Identify the blood parasite species.
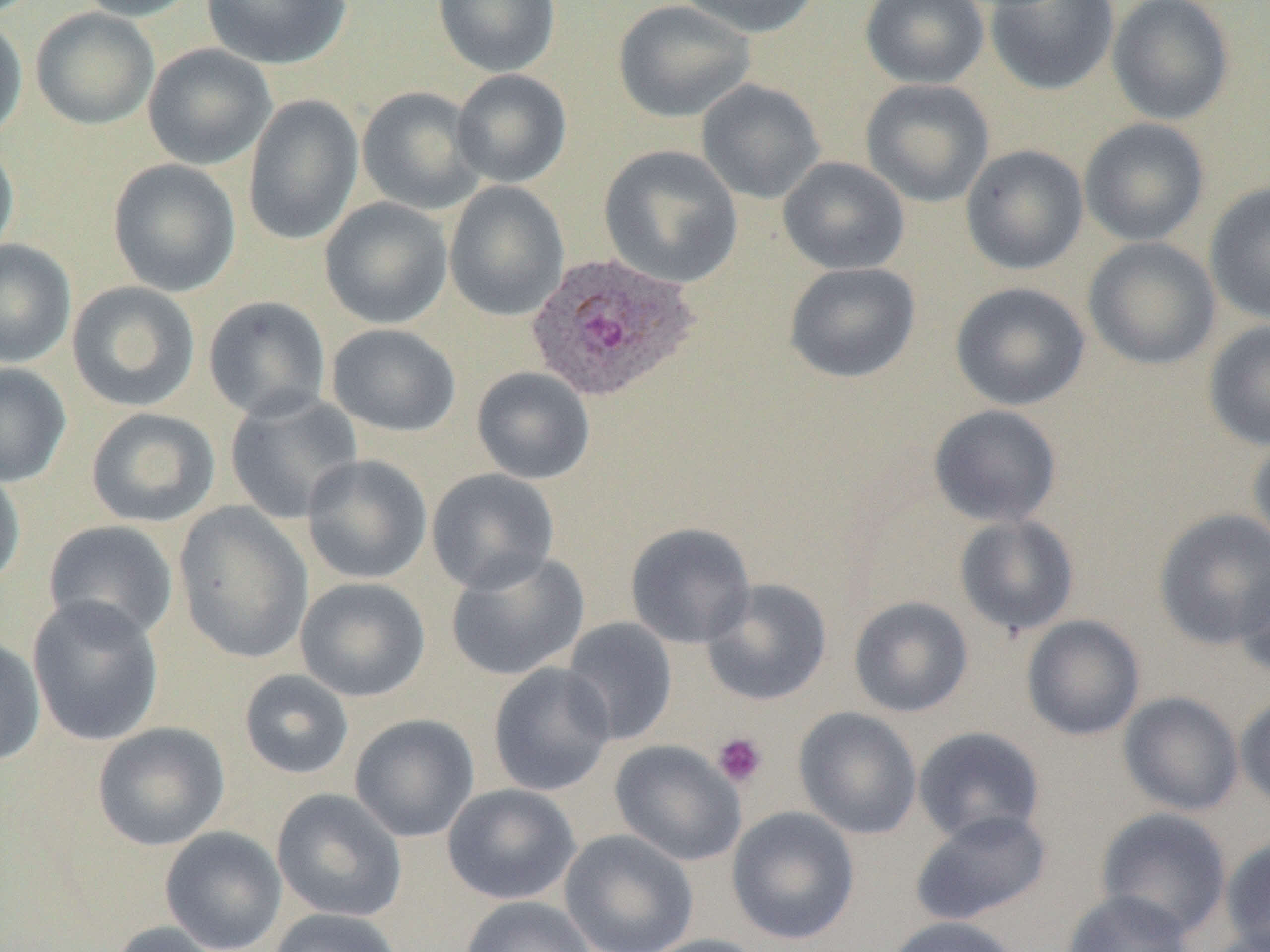

Plasmodium ovale.

Approximate bounding boxes as [x1, y1, x2, y2] in pixels. Plasmodium ovale-infected red blood cell locations: [526, 253, 697, 403]. Platelet locations: [711, 731, 768, 788]. Uninfected red blood cell locations: [71, 0, 202, 21], [201, 0, 352, 70], [432, 0, 561, 78], [674, 0, 822, 39], [860, 0, 990, 89], [985, 0, 1119, 96], [1107, 0, 1236, 126], [613, 1, 755, 123], [30, 8, 159, 130], [0, 13, 28, 145], [143, 43, 276, 170], [452, 69, 572, 188], [696, 79, 825, 204], [860, 79, 995, 209], [356, 86, 487, 215], [243, 95, 364, 245], [1079, 118, 1210, 247], [0, 135, 19, 264], [599, 144, 743, 288], [960, 144, 1089, 275], [777, 156, 910, 275], [107, 158, 241, 297], [444, 181, 570, 321], [1203, 183, 1270, 325], [320, 198, 453, 330], [1083, 236, 1222, 371], [0, 239, 77, 368], [784, 262, 921, 383], [66, 281, 201, 412], [950, 281, 1091, 411], [203, 296, 332, 422], [1203, 319, 1270, 451], [327, 324, 461, 437], [0, 362, 72, 487], [472, 367, 596, 485], [223, 389, 364, 524], [927, 403, 1063, 527], [85, 407, 221, 528], [1248, 433, 1270, 553], [301, 454, 433, 585], [0, 465, 26, 591], [426, 468, 560, 595], [172, 501, 313, 665], [1153, 508, 1270, 650], [954, 514, 1080, 638], [43, 519, 179, 643], [625, 521, 756, 649], [444, 549, 590, 681], [1234, 560, 1270, 682], [295, 577, 430, 702], [700, 578, 832, 706], [26, 595, 164, 746], [848, 596, 974, 717], [1021, 614, 1146, 741], [561, 617, 678, 746], [0, 634, 46, 768], [487, 662, 617, 797], [238, 669, 355, 779], [1118, 691, 1244, 816], [1235, 691, 1270, 813], [793, 707, 922, 839], [349, 714, 480, 843], [92, 722, 230, 851], [912, 726, 1047, 845], [610, 739, 746, 866], [442, 783, 581, 905], [271, 788, 407, 922], [726, 806, 860, 945], [1095, 807, 1232, 940], [908, 809, 1052, 926], [160, 826, 287, 952], [559, 829, 699, 952], [1220, 836, 1270, 952], [1061, 890, 1193, 952], [460, 896, 597, 952], [265, 908, 406, 952], [881, 916, 1024, 952], [104, 920, 229, 952], [637, 934, 771, 952]. Optical microscopy. Captured at 1000x magnification. Thin blood smear. Single field of view. Image is 1270×952 pixels.